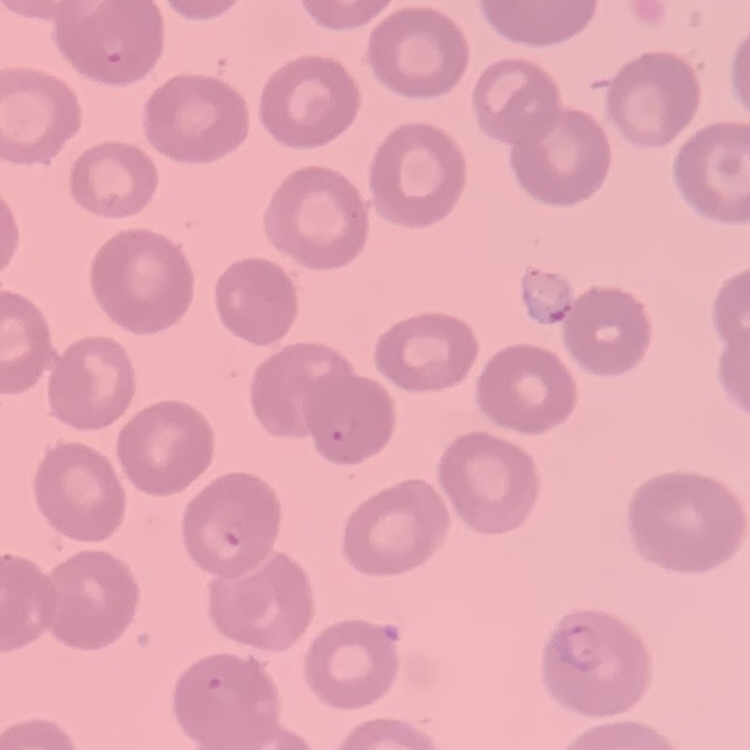
The red blood cells show no rouleaux formation. One tile cut from a larger photomicrograph. Thin blood smear. Field's or Giemsa stain.